Classify this cell by malaria status.
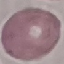
It is uninfected.

Summary:
  - Stain: Giemsa
  - Image type: cell patch, automatically extracted from a larger field of view and resized to 64 × 64 pixels
  - Preparation: thin smear
  - Capture: smartphone camera at the microscope eyepiece